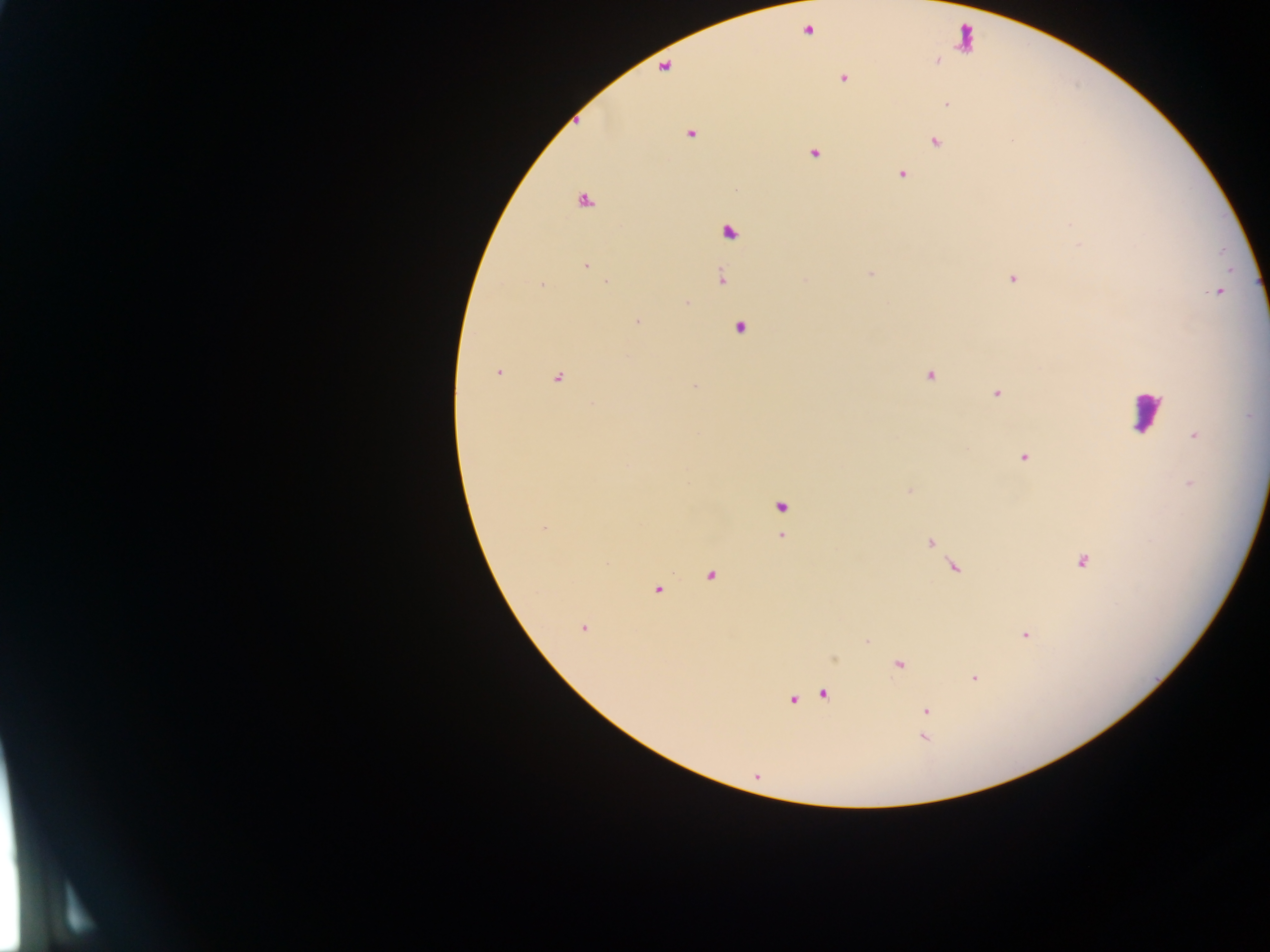

image size = 1270×952 pixels
capture = mobile-phone photograph through a microscope
country = Ghana
malaria parasite locations = approximate centers as (x, y) in pixels: (843, 79), (947, 104), (690, 134), (935, 142), (814, 153), (902, 174), (583, 203), (729, 233), (586, 266), (870, 274), (721, 278), (1013, 278), (606, 282), (541, 285), (1217, 292), (687, 302), (637, 322), (740, 328), (497, 372), (930, 376), (557, 378), (694, 386), (996, 394), (1194, 435), (1024, 457), (1190, 485), (781, 507), (544, 529), (780, 537), (930, 542), (1082, 561), (955, 567), (711, 576), (657, 590), (584, 628), (1025, 635), (899, 664), (974, 678), (823, 694), (793, 700), (925, 711), (923, 737)
leukocyte locations = approximate centers as (x, y) in pixels: (964, 39), (1147, 411)
field of view = single
preparation = thick blood film